Assess the morphology of the red blood cells.
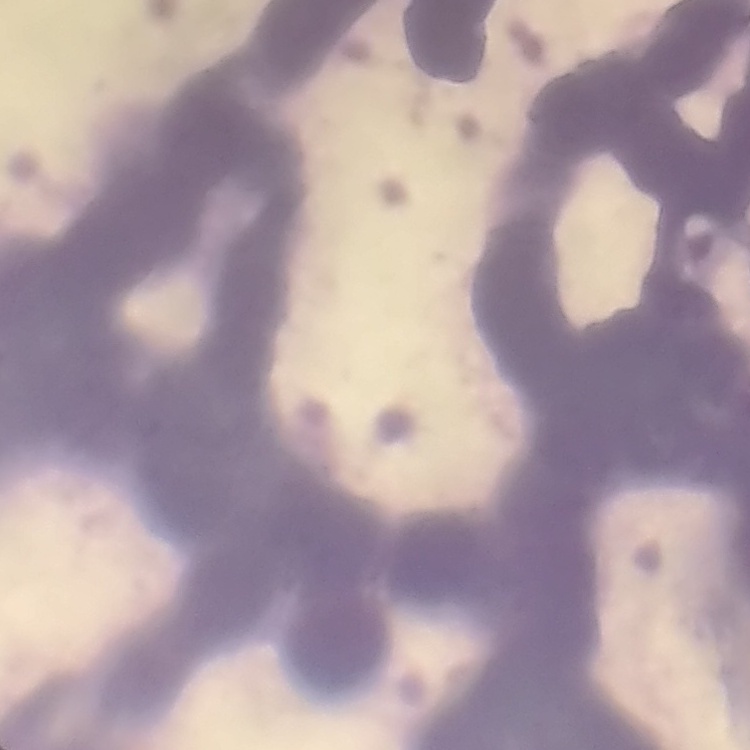
They show rouleaux formation.

Summary:
  - Stain: Field's or Giemsa
  - Preparation: thin peripheral smear
  - Image type: one tile cut from a larger photomicrograph